Point out every Plasmodium parasite.
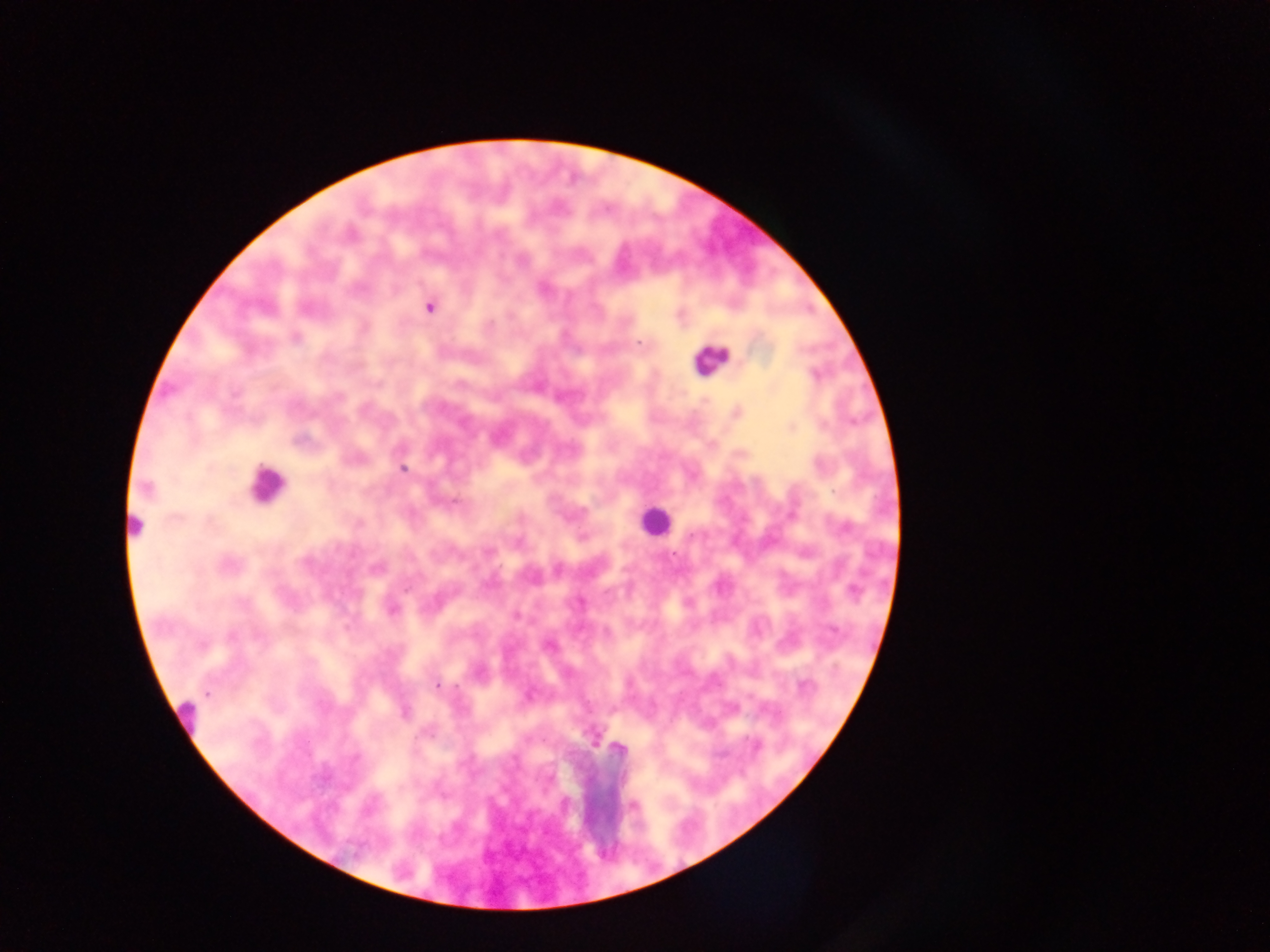
Approximate centers as (x, y) in pixels.
Plasmodium parasites: (429, 308), (296, 338), (638, 342), (816, 374), (339, 396), (402, 469), (146, 489), (455, 503), (359, 524), (583, 538), (487, 551), (674, 553), (227, 565), (406, 589), (853, 591), (392, 610), (517, 617), (231, 635), (259, 636), (202, 644), (438, 685), (207, 693), (404, 712), (756, 746).

Leukocyte locations: (710, 359), (266, 483), (655, 520), (132, 532), (183, 716). Single field of view. Collected in Ghana. Mobile-phone photograph taken through the microscope. Image is 1270×952 pixels. Thick blood film.